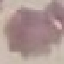

Malaria status: uninfected. Thin blood smear. Automatically extracted cell patch, resized to 64 × 64 pixels. Photographed with a smartphone camera at the microscope eyepiece. Giemsa stain.